Locate malaria parasites and leukocytes.
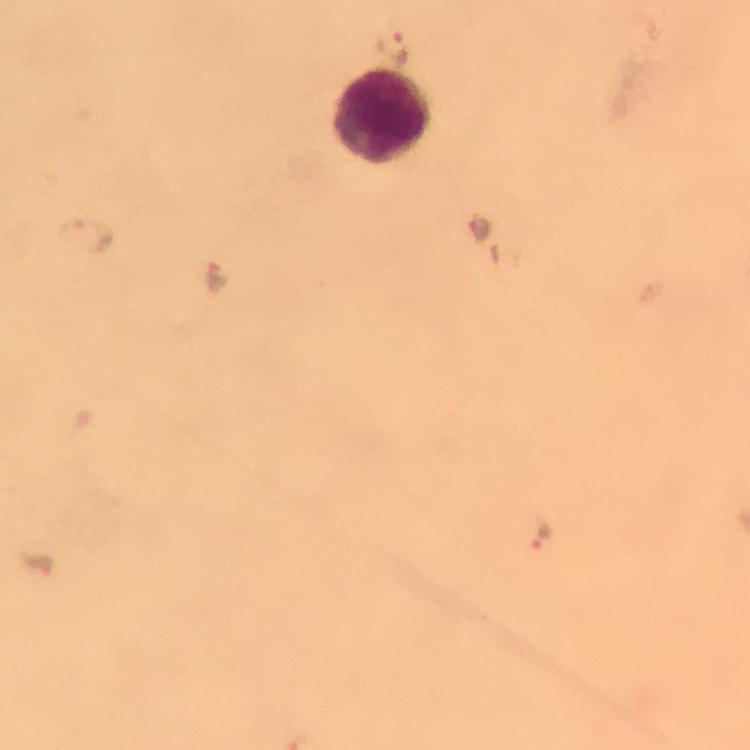

Approximate object centers, in pixels from the top-left corner.
Malaria parasites: (x=392, y=49), (x=480, y=230), (x=86, y=234), (x=215, y=275), (x=539, y=535), (x=40, y=562).
Leukocytes: (x=383, y=118).

{
  "magnification": "100x",
  "context": "from a malaria diagnostic workup",
  "immersion_oil": "applied",
  "capture": "smartphone camera through the microscope",
  "stain": "Giemsa",
  "image_size": "750×750 pixels",
  "cropped_from": "a single field of view",
  "preparation": "thick blood smear"
}